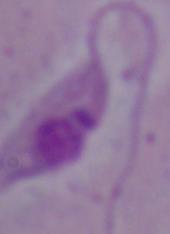

A Leishmania parasite is seen. 1000x magnification. Photomicrograph.